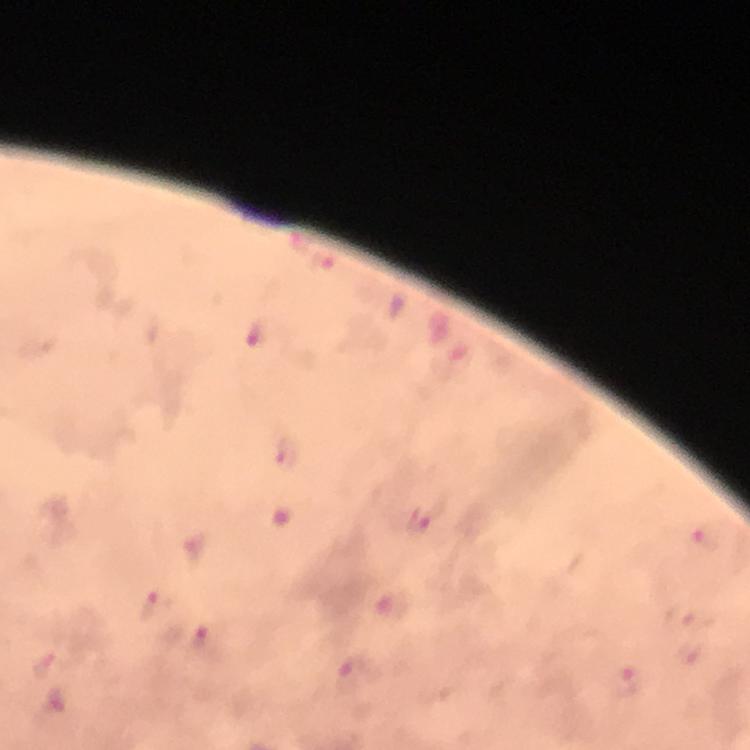
Approximate centers as {x, y} in pixels.
Summary:
  - Plasmodium parasite locations: {256, 336}, {290, 456}, {420, 518}, {704, 542}, {194, 550}, {392, 605}, {149, 606}, {680, 617}, {688, 651}, {357, 675}, {632, 680}
  - Context: from a diagnostic examination for malaria
  - Magnification: 100x
  - Stain: Giemsa
  - Immersion oil: used
  - Cropped from: one field of view
  - Preparation: thick smear
  - Image size: 750×750 pixels
  - Capture: smartphone photograph through a microscope